Comment on the morphology of the erythrocytes.
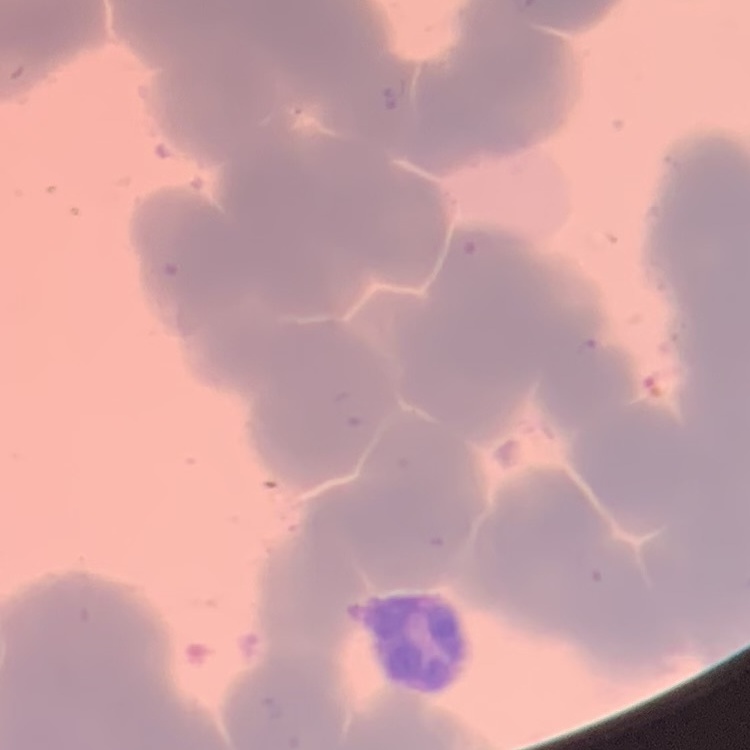

Rouleaux formation.

Field's or Giemsa stain. One tile cut from a larger photomicrograph. Thin blood smear.